Classify this cell by malaria status.
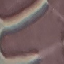
It is uninfected.

preparation = thin blood smear
capture = smartphone camera at the microscope eyepiece
stain = Giemsa
image type = automatically extracted cell patch, resized to 64 × 64 pixels